Locate and identify every blood parasite.
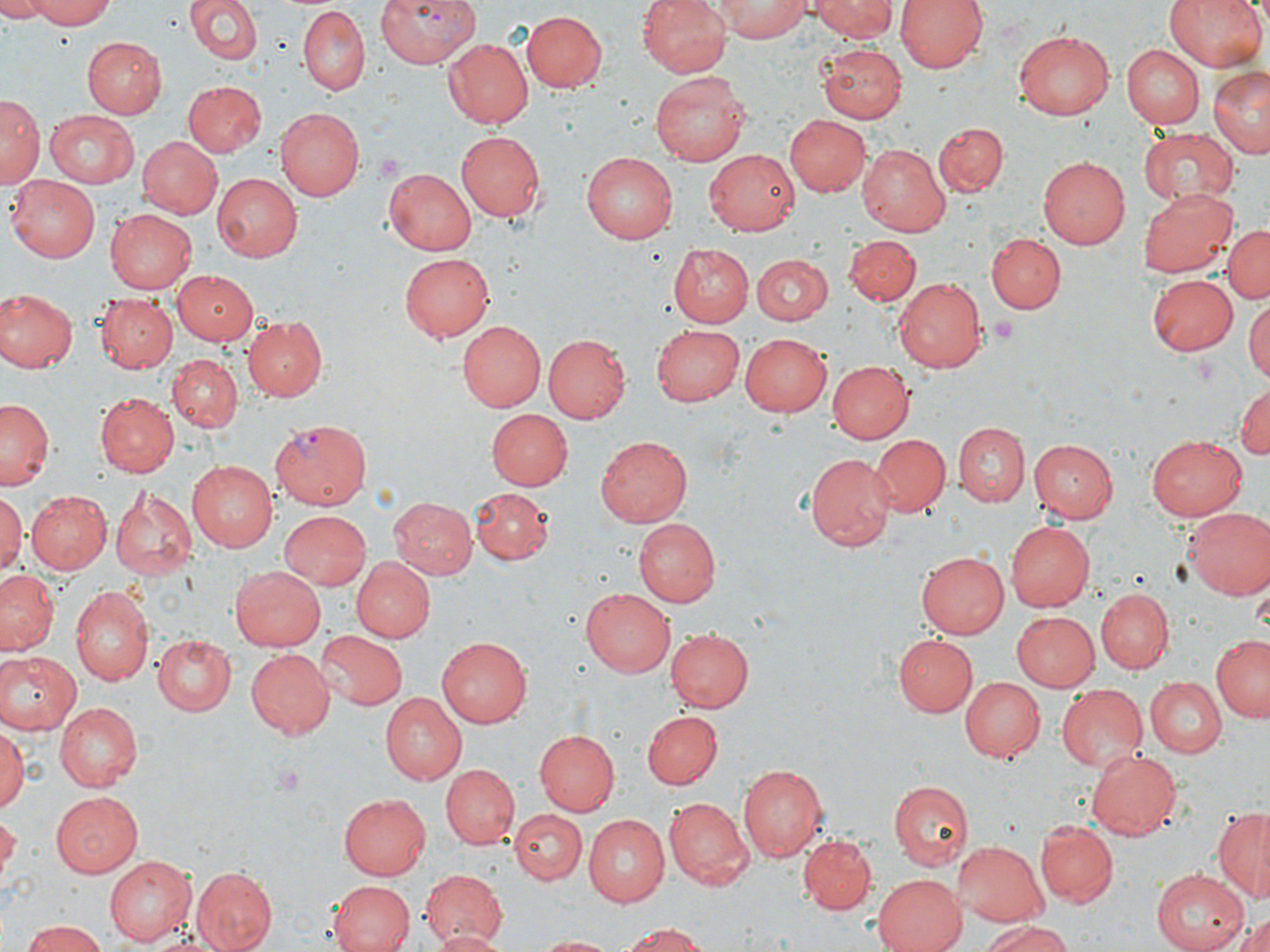
Approximate bounding boxes as [x1, y1, x2, y2] in pixels.
Plasmodium vivax-infected red blood cells: [376, 0, 476, 69], [268, 417, 370, 510].
No Plasmodium falciparum, Plasmodium ovale, Plasmodium malariae, Babesia divergens, or Trypanosoma brucei observed.

Uninfected red blood cell locations: [0, 0, 51, 22], [27, 0, 119, 27], [185, 0, 263, 66], [640, 0, 733, 76], [811, 0, 898, 43], [897, 0, 988, 73], [1163, 0, 1270, 73], [713, 1, 810, 41], [296, 6, 369, 96], [522, 9, 606, 93], [1012, 28, 1114, 120], [83, 37, 166, 118], [441, 38, 532, 128], [817, 43, 907, 123], [1122, 45, 1204, 128], [1209, 65, 1270, 159], [652, 72, 753, 165], [185, 80, 268, 157], [2, 94, 40, 186], [44, 108, 143, 187], [276, 108, 364, 201], [784, 114, 870, 196], [934, 122, 1007, 196], [1138, 125, 1240, 206], [455, 129, 545, 219], [137, 137, 223, 219], [226, 141, 342, 254], [857, 144, 951, 236], [705, 150, 800, 236], [581, 152, 678, 242], [1039, 155, 1129, 250], [385, 166, 480, 255], [212, 173, 302, 262], [8, 176, 102, 262], [1141, 186, 1237, 278], [105, 207, 197, 291], [1223, 224, 1269, 306], [986, 233, 1063, 313], [844, 235, 921, 305], [668, 245, 753, 327], [400, 252, 495, 341], [750, 255, 832, 326], [171, 270, 260, 343], [1148, 275, 1239, 357], [894, 278, 987, 372], [0, 287, 77, 374], [94, 293, 178, 374], [1245, 296, 1270, 384], [243, 316, 329, 401], [455, 321, 544, 411], [650, 324, 744, 407], [739, 332, 832, 417], [542, 335, 630, 423], [168, 353, 243, 433], [825, 360, 912, 444], [1233, 381, 1270, 463], [94, 393, 178, 477], [0, 397, 53, 491], [487, 409, 573, 489], [954, 423, 1030, 507], [870, 433, 951, 516], [1145, 435, 1248, 520], [595, 436, 693, 527], [1028, 438, 1118, 522], [805, 453, 894, 551], [185, 459, 276, 552], [109, 484, 198, 583], [468, 487, 555, 566], [24, 490, 112, 574], [0, 494, 24, 578], [390, 497, 477, 580], [1183, 506, 1269, 600], [278, 511, 371, 591], [633, 518, 719, 607], [1007, 522, 1093, 611], [915, 550, 1007, 639], [350, 557, 433, 643], [230, 565, 326, 651], [0, 569, 57, 655], [71, 585, 153, 685], [580, 586, 675, 675], [1096, 587, 1174, 672], [1010, 611, 1098, 692], [665, 629, 753, 714], [314, 630, 405, 709], [1212, 631, 1269, 724], [894, 633, 977, 716], [153, 635, 237, 714], [436, 636, 531, 726], [246, 649, 335, 738], [0, 652, 78, 735], [963, 675, 1045, 763], [1145, 677, 1224, 756], [1056, 683, 1147, 771], [378, 693, 466, 785], [55, 702, 142, 790], [642, 712, 722, 789], [0, 728, 25, 814], [533, 728, 620, 815], [1086, 748, 1182, 840], [738, 762, 827, 862], [441, 764, 518, 848], [889, 779, 973, 868], [49, 790, 144, 877], [339, 792, 431, 880], [662, 796, 752, 888], [1212, 807, 1270, 903], [332, 808, 423, 952], [511, 809, 587, 885], [581, 816, 669, 907], [1, 817, 18, 877], [1035, 822, 1116, 907], [799, 836, 876, 914], [951, 842, 1051, 925], [104, 855, 196, 945], [190, 867, 277, 951], [1152, 869, 1251, 951], [418, 870, 509, 947], [869, 873, 967, 952], [328, 880, 415, 952], [1224, 910, 1270, 952], [977, 919, 1074, 952], [21, 921, 107, 952], [616, 921, 707, 952], [427, 929, 507, 952], [532, 934, 626, 951]. Platelet locations: [373, 151, 404, 178], [987, 316, 1019, 348], [269, 763, 307, 795]. Slide-level diagnosis: Plasmodium vivax. Optical microscopy. May-Grünwald-Giemsa stain. Single field of view. Captured at 1000x magnification. Thin blood smear. Image is 1270×952 pixels.